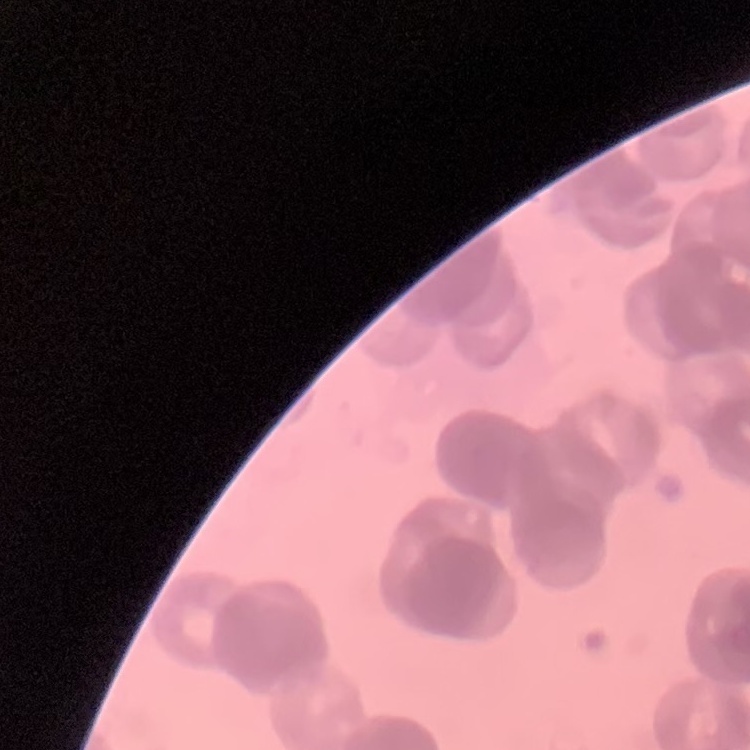

The erythrocytes exhibit rouleaux formation. Field's or Giemsa stain. Thin blood film. One tile cut from a larger photomicrograph.